Report the malaria status of this cell.
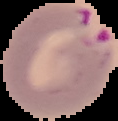

Parasitized.

Summary:
  - Preparation: thin blood film
  - Image size: 118×121 pixels
  - Image type: segmented cell region with the area outside set to black